Identify the parasite.
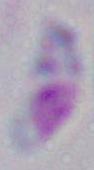

This is Toxoplasma gondii.

magnification: 1000x
modality: photomicrograph